Find each parasitized red blood cell.
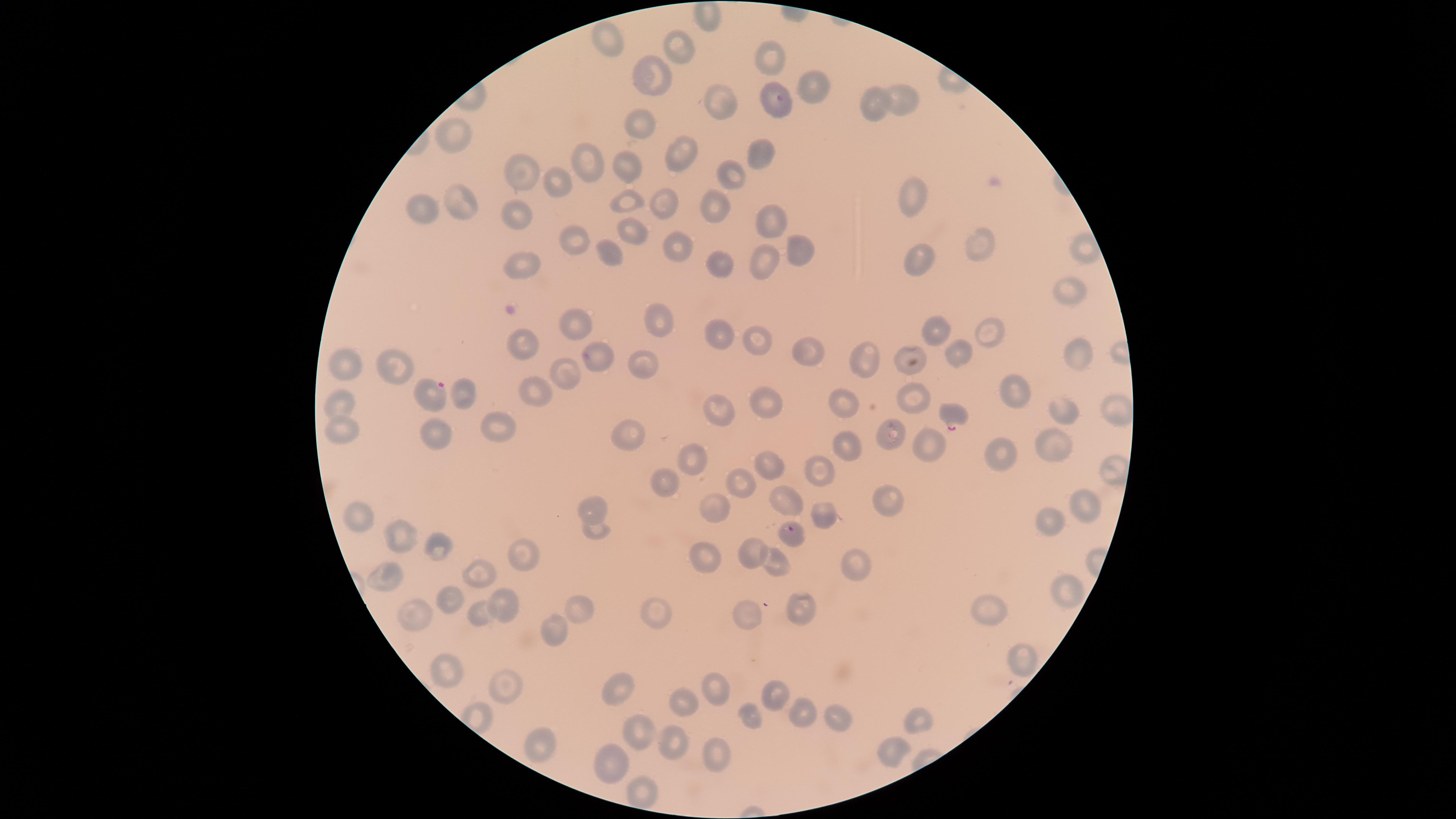

Approximate marker points as (x, y) in pixels.
Parasitized red blood cells: (435, 392), (954, 416), (791, 530).

Approximate marker points as (x, y) in pixels.
Summary:
  - Uninfected red blood cells: (613, 43), (684, 47), (773, 55), (654, 70), (815, 85), (713, 98), (869, 100), (903, 100), (775, 102), (640, 126), (459, 135), (683, 147), (759, 152), (593, 166), (624, 167), (530, 172), (726, 174), (560, 177), (915, 196), (458, 198), (664, 199), (621, 203), (712, 206), (425, 207), (767, 217), (520, 220), (633, 229), (980, 237), (578, 242), (793, 245), (673, 247), (613, 251), (1083, 252), (918, 260), (526, 262), (710, 262), (766, 264), (1068, 291), (937, 326), (573, 327), (656, 327), (989, 328), (721, 336), (756, 337), (525, 347), (1077, 348), (814, 350), (957, 352), (594, 353), (868, 359), (903, 361), (397, 362), (638, 364), (348, 368), (571, 380), (535, 391), (1019, 394), (914, 397), (344, 399), (775, 403), (841, 404), (1116, 407), (721, 408), (1063, 413), (629, 425), (342, 426), (506, 426), (446, 428), (894, 435), (849, 444), (931, 447), (1055, 448), (696, 457), (997, 459), (762, 460), (817, 470), (665, 478), (737, 485), (790, 494), (887, 501), (596, 505), (1083, 509), (829, 514), (359, 515), (715, 515), (1049, 517), (594, 528), (396, 537), (438, 546), (519, 551), (702, 553), (753, 554), (856, 560), (778, 566), (476, 572), (390, 576), (1066, 589), (453, 597), (507, 602), (581, 604), (802, 604), (655, 607), (483, 612), (988, 612), (416, 616), (750, 623), (559, 630), (1018, 654), (453, 672), (620, 684), (718, 684), (504, 685), (774, 690), (679, 697), (749, 706), (805, 713), (919, 714), (841, 717), (643, 729), (676, 738), (541, 742), (891, 743), (717, 752), (613, 761), (636, 790)
  - Stain: Giemsa
  - Field of view: single
  - Species: Plasmodium falciparum
  - Preparation: thin blood film
  - Capture: smartphone photograph through the microscope eyepiece
  - Visible region: circular
  - Image size: 1456×819 pixels